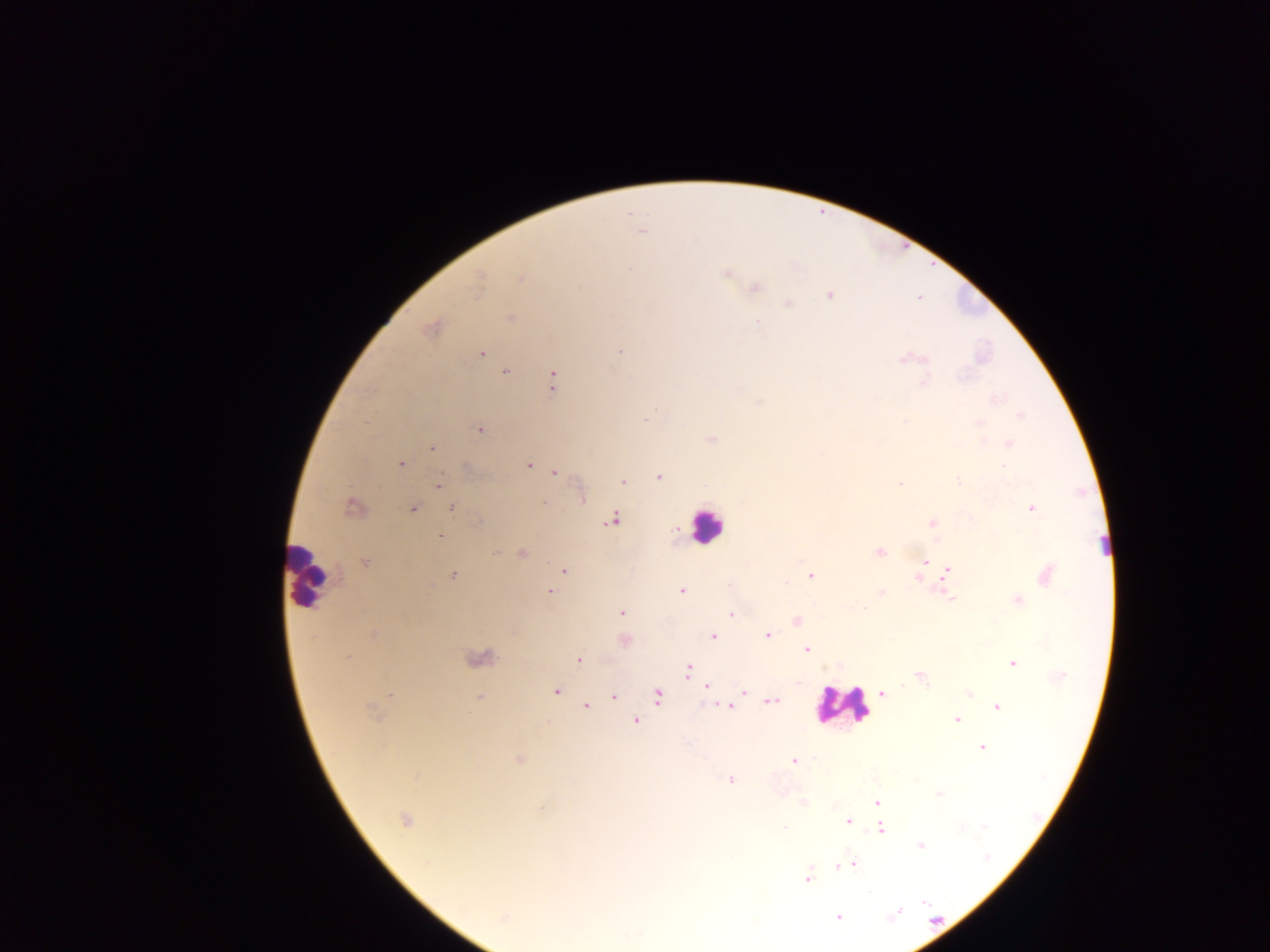
Approximate centers as [x, y] in pixels.
Summary:
  - Leukocyte locations: [705, 525], [307, 575], [840, 706]
  - Malaria parasite locations: [641, 231], [630, 269], [727, 273], [520, 278], [479, 279], [756, 287], [829, 295], [788, 303], [511, 318], [431, 329], [620, 351], [481, 353], [903, 359], [505, 372], [553, 380], [924, 381], [1021, 415], [645, 418], [479, 429], [711, 438], [1009, 443], [431, 448], [401, 463], [529, 465], [555, 473], [659, 477], [958, 481], [623, 482], [439, 483], [899, 484], [582, 498], [353, 507], [452, 508], [1032, 508], [414, 509], [611, 519], [932, 523], [440, 537], [879, 552], [522, 553], [924, 562], [366, 563], [564, 570], [948, 573], [453, 574], [1046, 575], [810, 576], [917, 578], [729, 586], [549, 590], [682, 591], [881, 592], [951, 599], [1019, 600], [621, 613], [732, 614], [797, 621], [374, 635], [767, 635], [714, 636], [807, 649], [348, 657], [579, 659], [1013, 664], [689, 669], [921, 678], [706, 687], [556, 691], [744, 691], [882, 693], [969, 693], [390, 695], [658, 695], [614, 697], [479, 698], [773, 702], [586, 706], [728, 706], [998, 707], [371, 711], [957, 720], [637, 722], [982, 747], [519, 759], [794, 761], [730, 780], [939, 794], [877, 802], [804, 804], [542, 809], [405, 819], [848, 821], [784, 827], [881, 829], [921, 845], [853, 864], [841, 866], [807, 879], [925, 903], [897, 914], [838, 917], [503, 918]
  - Capture: mobile-phone photograph through a microscope
  - Field of view: single
  - Image size: 1270×952 pixels
  - Country: Ghana
  - Preparation: thick blood smear